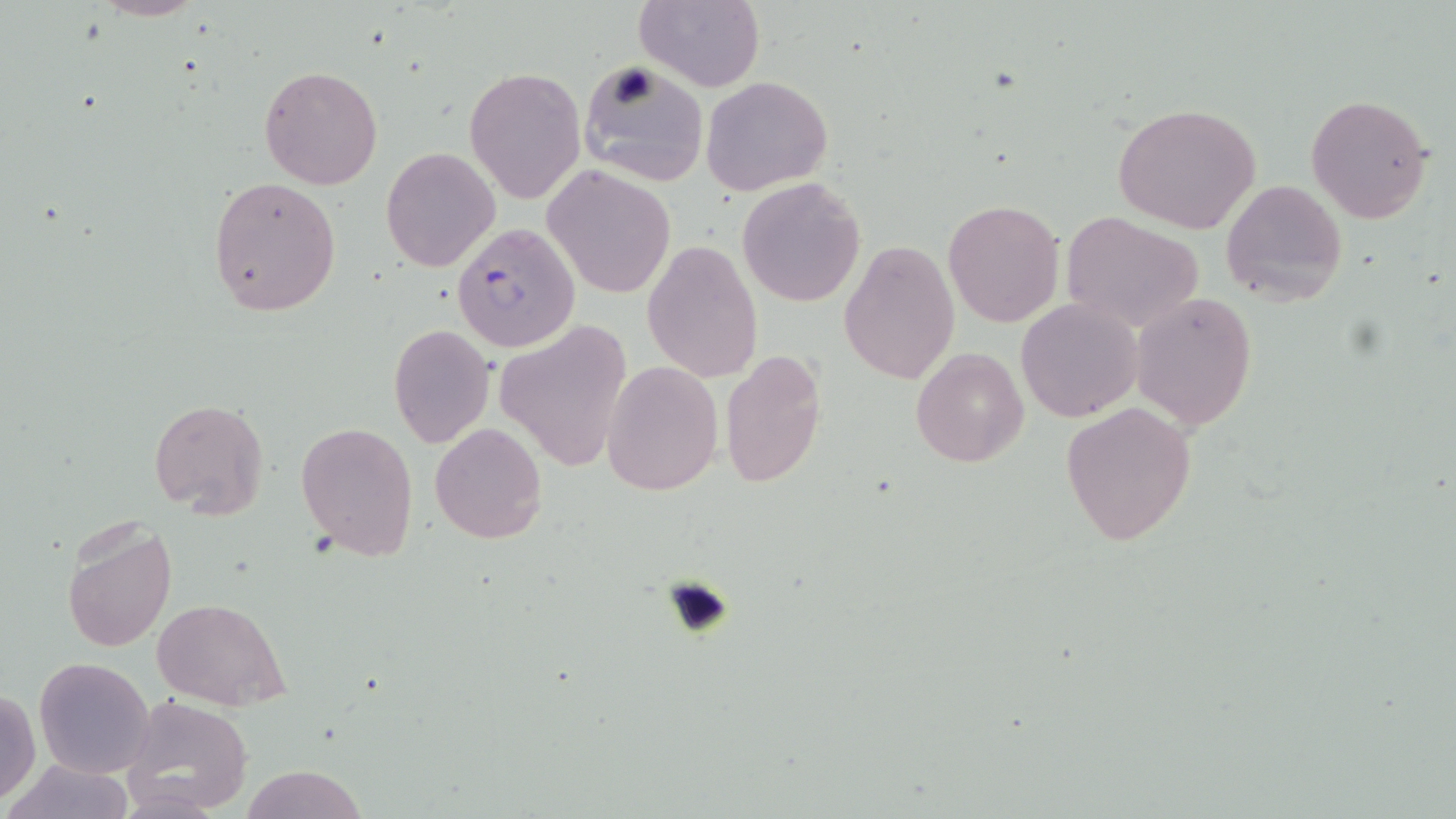
Summary:
  - Coordinate format: approximate bounding boxes as (x1, y1, x2, y2) in pixels
  - Plasmodium falciparum-infected red blood cell locations: (453, 221, 582, 353)
  - Uninfected red blood cell locations: (93, 0, 206, 21), (635, 0, 765, 92), (576, 59, 709, 185), (259, 65, 384, 190), (464, 66, 586, 203), (701, 74, 833, 196), (1305, 93, 1435, 225), (1114, 101, 1263, 234), (380, 146, 500, 272), (543, 164, 676, 300), (207, 177, 341, 316), (737, 177, 866, 307), (1221, 177, 1348, 307), (943, 200, 1064, 328), (1061, 212, 1206, 334), (840, 240, 959, 385), (643, 241, 762, 382), (1130, 292, 1257, 430), (1014, 298, 1143, 421), (495, 318, 633, 473), (388, 322, 494, 449), (910, 346, 1030, 469), (719, 349, 828, 487), (604, 361, 723, 498), (149, 398, 267, 518), (1060, 402, 1198, 547), (295, 421, 418, 559), (430, 422, 547, 544), (61, 515, 176, 654), (156, 598, 289, 711), (33, 656, 154, 779), (1, 688, 41, 804), (126, 696, 253, 814), (6, 760, 136, 819), (241, 766, 367, 819)
  - Slide-level diagnosis: Plasmodium falciparum
  - Magnification: 1000x
  - Image size: 1456×819 pixels
  - Modality: optical microscopy
  - Preparation: thin blood smear
  - Field of view: single
  - Stain: May-Grünwald-Giemsa